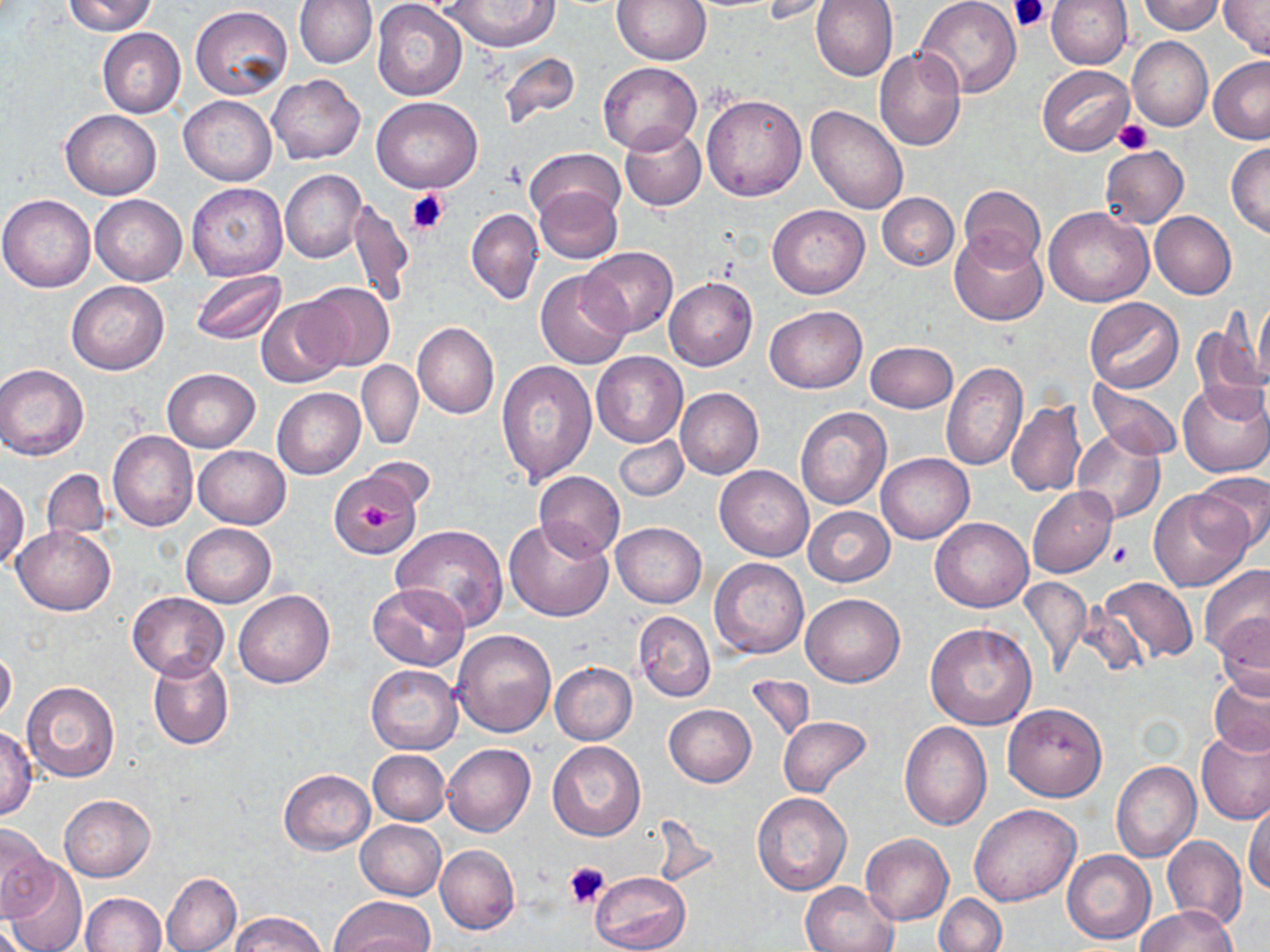
Summary:
  - Coordinate format: approximate bounding boxes as (x1, y1, x2, y2) in pixels
  - Uninfected red blood cell locations: (64, 0, 158, 35), (292, 0, 374, 144), (294, 0, 377, 68), (612, 0, 709, 65), (811, 0, 897, 81), (916, 0, 1021, 98), (1045, 0, 1132, 68), (1136, 0, 1224, 34), (762, 1, 840, 23), (1220, 1, 1270, 59), (443, 2, 558, 52), (372, 3, 467, 101), (191, 6, 293, 101), (97, 28, 186, 118), (1127, 37, 1213, 131), (874, 47, 964, 151), (498, 51, 580, 127), (1208, 57, 1270, 145), (597, 61, 703, 154), (1037, 65, 1134, 156), (267, 74, 365, 165), (702, 94, 807, 200), (179, 95, 276, 185), (371, 97, 482, 194), (805, 106, 908, 214), (60, 109, 162, 199), (619, 125, 706, 210), (1225, 143, 1270, 238), (1100, 146, 1189, 228), (526, 147, 624, 225), (280, 171, 367, 263), (185, 182, 288, 281), (960, 184, 1045, 269), (535, 187, 623, 264), (877, 193, 958, 271), (0, 194, 96, 292), (90, 195, 186, 285), (348, 200, 413, 309), (767, 203, 869, 298), (1044, 206, 1153, 307), (466, 208, 543, 303), (1150, 210, 1236, 298), (949, 230, 1048, 327), (581, 247, 678, 336), (535, 269, 631, 369), (190, 271, 286, 346), (664, 277, 757, 370), (66, 280, 169, 375), (298, 281, 395, 372), (256, 297, 349, 387), (1084, 298, 1183, 393), (1253, 299, 1270, 385), (764, 306, 866, 393), (1191, 322, 1268, 420), (413, 323, 498, 418), (865, 341, 957, 412), (591, 352, 687, 448), (357, 360, 423, 449), (496, 361, 596, 485), (941, 361, 1026, 470), (0, 364, 89, 460), (162, 368, 259, 451), (1089, 380, 1185, 460), (1178, 381, 1270, 479), (675, 387, 763, 480), (272, 388, 366, 479), (1005, 401, 1086, 498), (795, 406, 891, 510), (1072, 428, 1165, 527), (108, 431, 198, 532), (613, 435, 689, 502), (194, 446, 290, 528), (877, 453, 973, 544), (359, 457, 436, 513), (715, 465, 814, 561), (40, 469, 111, 541), (533, 470, 624, 560), (1190, 470, 1270, 556), (326, 475, 418, 553), (0, 479, 28, 568), (1026, 487, 1118, 577), (1149, 488, 1253, 592), (803, 506, 895, 586), (504, 518, 613, 621), (930, 518, 1032, 612), (611, 522, 707, 607), (180, 523, 276, 607), (14, 526, 115, 614), (392, 526, 509, 631), (708, 557, 809, 658), (1199, 564, 1270, 660), (1020, 576, 1090, 676), (1098, 576, 1198, 664), (369, 583, 469, 670), (233, 589, 335, 688), (800, 591, 904, 686), (127, 592, 229, 679), (634, 611, 715, 701), (1215, 615, 1270, 702), (923, 623, 1036, 731), (451, 629, 557, 737), (0, 646, 16, 725), (148, 656, 233, 750), (550, 662, 637, 744), (366, 664, 462, 754), (744, 674, 816, 743), (1209, 676, 1270, 757), (22, 682, 120, 784), (1002, 703, 1107, 801), (664, 704, 756, 787), (778, 716, 873, 799), (899, 721, 992, 828), (0, 727, 38, 818), (1196, 727, 1270, 823), (546, 740, 646, 840), (442, 743, 534, 836), (368, 750, 450, 826), (1112, 762, 1200, 862), (279, 769, 375, 854), (752, 793, 852, 896), (60, 795, 155, 881), (1244, 799, 1270, 896), (969, 803, 1081, 906), (647, 815, 719, 889), (356, 820, 446, 899), (0, 824, 57, 919), (861, 833, 954, 925), (1162, 835, 1245, 932), (435, 845, 519, 934), (1062, 849, 1154, 945), (4, 859, 86, 952), (590, 872, 691, 952), (161, 873, 241, 952), (800, 881, 898, 952), (81, 892, 166, 952), (935, 894, 1006, 952), (329, 897, 433, 952), (1134, 905, 1237, 952), (229, 912, 329, 952)
  - Platelet locations: (1009, 0, 1050, 34), (1114, 120, 1152, 155), (405, 188, 448, 234), (356, 501, 393, 533), (1110, 543, 1134, 567), (565, 862, 611, 908)
  - Slide-level diagnosis: no evidence of blood parasites
  - Stain: May-Grünwald-Giemsa
  - Image size: 1270×952 pixels
  - Preparation: thin blood film
  - Magnification: 1000x
  - Field of view: single
  - Modality: light microscopy